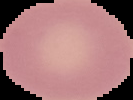

Summary:
  - Result: no malaria parasites detected
  - Preparation: thin blood film
  - Image type: cell region segmented out of the field of view; surrounding area masked to black
  - Image size: 133×100 pixels